Assess this cell for malaria.
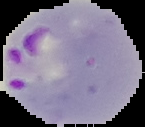
It is parasitized.

preparation = thin blood film
image type = segmented cell region with the area outside set to black
image size = 145×127 pixels